Name the cell type shown.
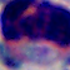
This is a leukocyte.

1000x magnification. Micrograph.